Locate every blood parasite and identify its species.
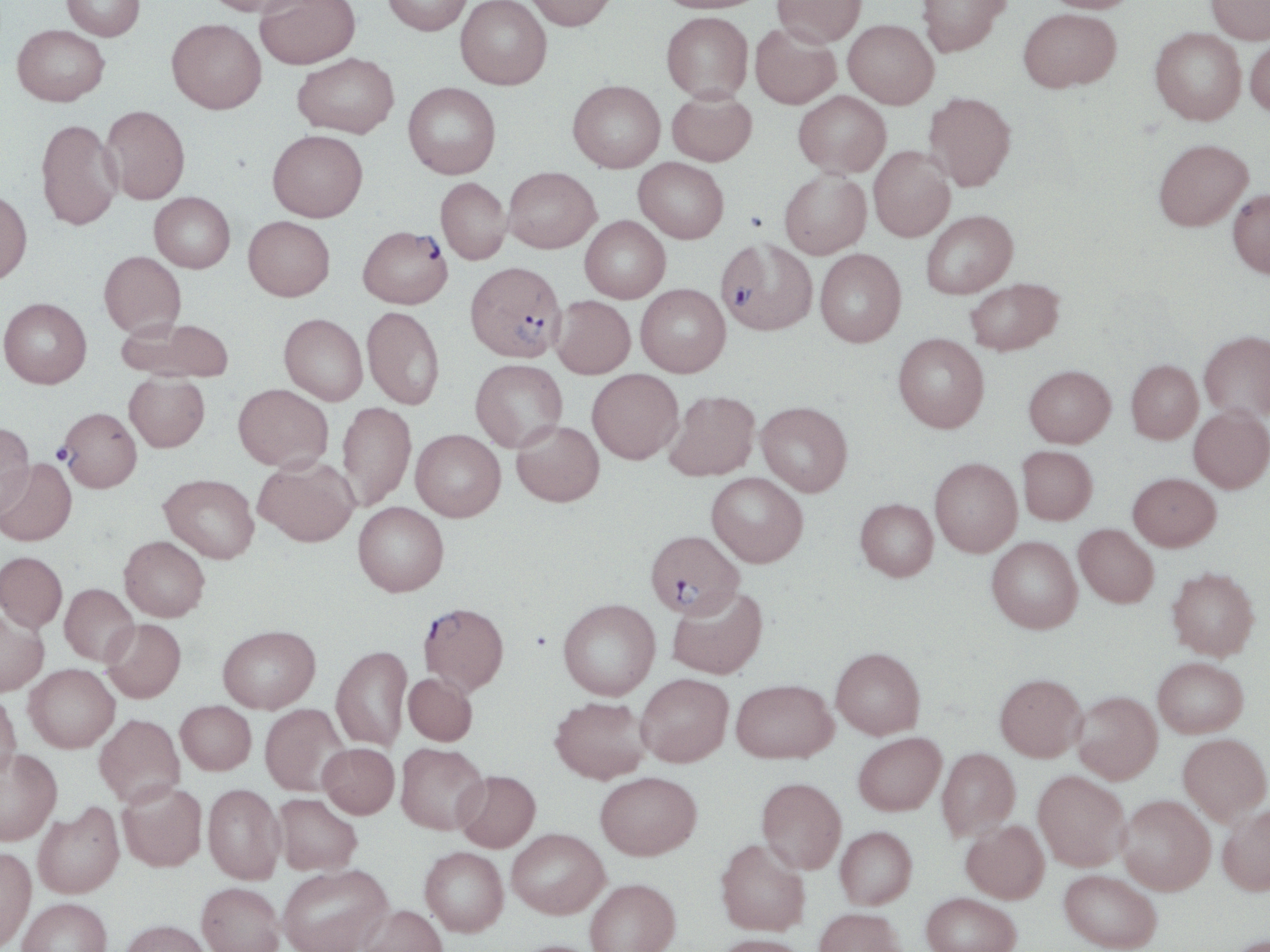

Approximate bounding boxes as (x1,y1)-(x2,y2) corner pairs in pixels.
Plasmodium falciparum-infected red blood cells: (358,226)-(452,309), (716,237)-(817,335), (464,260)-(566,362), (60,408)-(140,491), (646,530)-(744,618), (418,601)-(509,695).
No Plasmodium ovale, Plasmodium malariae, Plasmodium vivax, Babesia divergens, or Trypanosoma brucei observed.

Uninfected red blood cell locations: (62,0)-(145,40), (203,0)-(313,17), (255,0)-(360,69), (382,0)-(472,35), (455,0)-(551,89), (524,0)-(616,31), (654,0)-(767,13), (772,0)-(867,47), (916,0)-(1011,57), (1040,0)-(1142,13), (1206,0)-(1270,44), (1018,8)-(1121,92), (661,11)-(753,102), (167,19)-(266,114), (843,19)-(939,109), (750,23)-(842,109), (12,24)-(109,106), (1150,27)-(1246,124), (1245,36)-(1270,116), (292,52)-(398,138), (568,80)-(665,172), (403,82)-(501,179), (667,89)-(757,166), (793,91)-(891,177), (924,92)-(1017,191), (101,105)-(190,204), (36,119)-(123,230), (268,129)-(367,221), (1153,138)-(1253,230), (869,146)-(955,242), (634,158)-(729,243), (503,167)-(601,253), (779,169)-(871,258), (436,177)-(511,264), (1228,188)-(1270,278), (0,190)-(32,284), (149,192)-(235,272), (921,210)-(1017,299), (580,215)-(670,302), (243,216)-(335,301), (815,249)-(905,347), (99,251)-(186,337), (965,278)-(1063,355), (636,284)-(730,377), (550,296)-(635,378), (0,297)-(92,388), (362,306)-(445,410), (279,314)-(368,404), (118,317)-(236,383), (1199,330)-(1270,421), (893,333)-(989,432), (470,359)-(568,451), (1126,359)-(1202,444), (1024,365)-(1115,447), (587,369)-(683,464), (124,373)-(210,452), (233,383)-(333,471), (664,390)-(760,481), (337,401)-(416,510), (756,401)-(853,496), (1189,407)-(1270,493), (512,421)-(604,506), (0,422)-(35,519), (411,430)-(505,521), (1018,446)-(1097,524), (253,457)-(358,546), (0,458)-(77,547), (930,458)-(1022,557), (707,472)-(807,567), (1128,473)-(1221,551), (160,474)-(259,563), (855,498)-(938,581), (352,502)-(449,596), (1074,523)-(1158,607), (119,536)-(210,621), (987,536)-(1082,633), (0,551)-(67,632), (1167,566)-(1260,660), (59,583)-(139,666), (666,585)-(768,680), (558,598)-(660,699), (0,606)-(49,696), (100,618)-(186,702), (218,624)-(320,713), (331,645)-(412,751), (831,647)-(925,739), (1153,657)-(1249,737), (24,664)-(119,752), (403,672)-(478,746), (636,673)-(733,766), (995,673)-(1087,761), (731,679)-(838,763), (1072,691)-(1162,783), (0,692)-(22,782), (549,696)-(651,784), (176,701)-(256,775), (260,703)-(349,796), (94,713)-(185,807), (853,732)-(946,815), (1178,733)-(1270,824), (318,742)-(399,819), (396,742)-(489,834), (937,747)-(1019,840), (0,749)-(62,846), (454,770)-(541,852), (1033,770)-(1130,870), (596,771)-(702,859), (756,777)-(846,873), (117,781)-(208,871), (203,783)-(285,884), (272,793)-(362,875), (1118,794)-(1215,894), (33,802)-(125,898), (1217,803)-(1270,895), (962,819)-(1050,903), (835,826)-(917,909), (507,828)-(609,918), (716,838)-(809,935), (420,846)-(509,936), (0,847)-(36,949), (277,863)-(393,952), (1059,869)-(1162,951), (585,878)-(680,952), (196,882)-(285,952), (921,892)-(1021,952), (17,897)-(112,952), (355,904)-(448,952), (813,907)-(905,952), (120,919)-(213,952), (713,934)-(809,952), (511,939)-(602,952). Platelet locations: (530,630)-(552,650). Slide-level diagnosis: Plasmodium falciparum. Optical microscopy. Image is 1270×952 pixels. Thin blood smear. Captured at 1000x magnification. May-Grünwald-Giemsa stain. One field of a larger specimen.